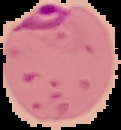 Malaria status: parasitized. From a thin blood film. Cell region segmented out of the field of view; the surrounding area is masked to black. Image is 121×130 pixels.